Outline every malaria parasite.
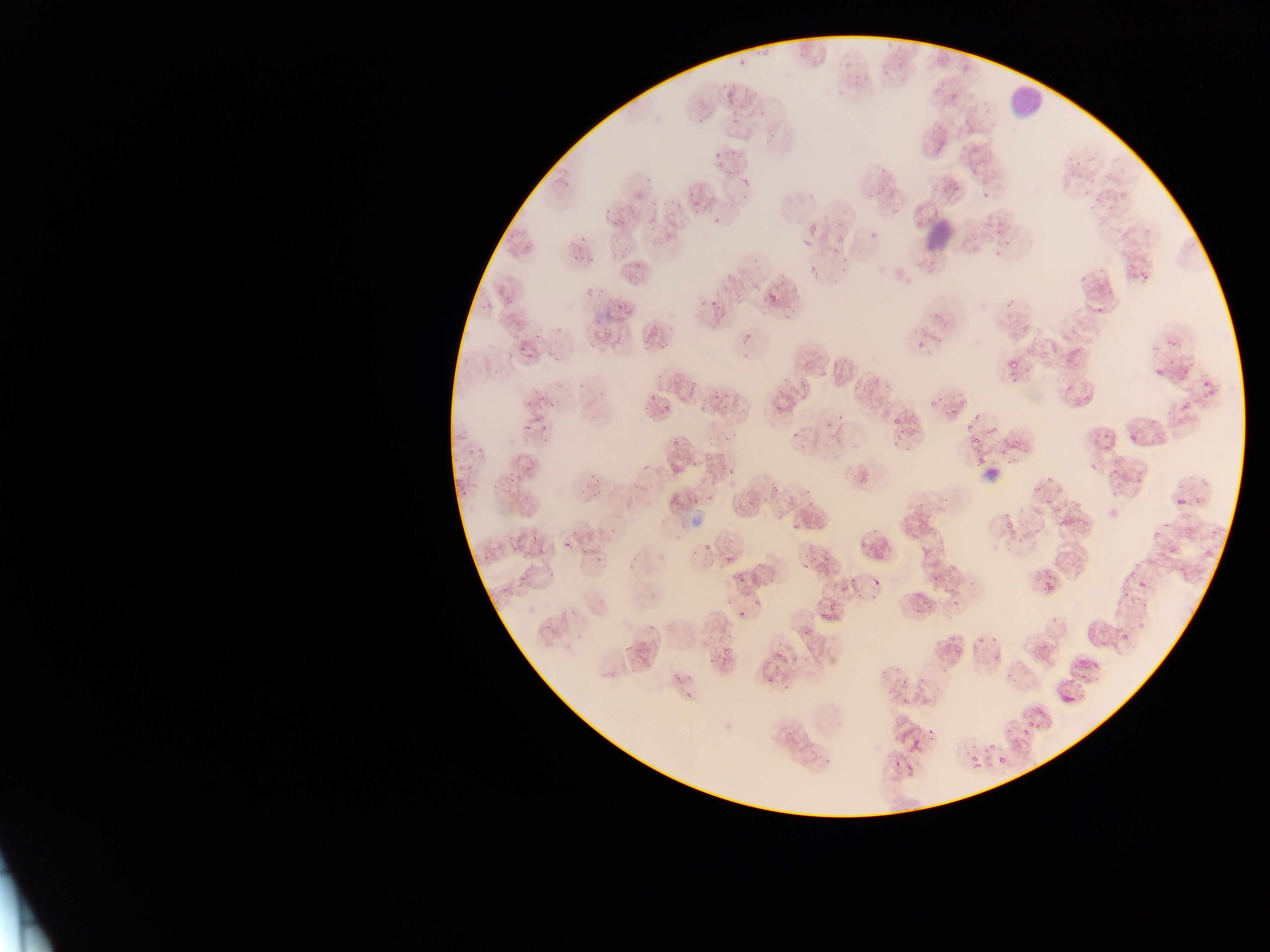
Approximate bounding boxes as (left, top, right, bottom) in pixels.
Malaria parasites: (948, 84, 976, 108), (1066, 153, 1088, 171), (637, 180, 671, 208), (687, 193, 706, 211), (978, 193, 986, 203), (794, 210, 827, 248), (604, 212, 622, 234), (714, 213, 728, 230), (661, 222, 685, 236), (986, 223, 1018, 244), (513, 231, 534, 266), (610, 244, 632, 260), (569, 249, 582, 263), (620, 276, 644, 287), (493, 281, 522, 318), (761, 286, 786, 303), (710, 295, 717, 306), (594, 314, 618, 335), (739, 322, 761, 336), (644, 324, 657, 338), (551, 338, 568, 352), (1172, 338, 1202, 378), (1145, 341, 1176, 379), (516, 343, 532, 357), (1005, 351, 1026, 377), (493, 352, 517, 379), (777, 372, 816, 401), (852, 379, 862, 391), (1179, 384, 1197, 416), (1200, 384, 1222, 402), (531, 389, 556, 416), (707, 394, 729, 412), (654, 396, 671, 410), (927, 396, 937, 408), (968, 396, 988, 430), (771, 400, 785, 413), (828, 408, 845, 427), (888, 408, 906, 438), (518, 418, 533, 437), (1125, 426, 1139, 450), (966, 429, 980, 446), (669, 434, 679, 446), (704, 445, 714, 459), (497, 450, 539, 496), (968, 451, 986, 476), (1103, 451, 1134, 473), (459, 459, 471, 483), (729, 459, 739, 476), (1026, 472, 1061, 498), (772, 478, 782, 491), (588, 479, 603, 497), (912, 485, 942, 509), (1172, 495, 1191, 510), (786, 512, 806, 536), (998, 512, 1021, 535), (924, 514, 937, 536), (508, 531, 529, 549), (700, 538, 718, 554), (562, 540, 573, 552), (590, 547, 616, 563), (804, 550, 820, 561), (926, 561, 954, 598), (1042, 563, 1072, 589), (1132, 566, 1156, 588), (871, 571, 889, 586), (734, 573, 744, 583), (841, 582, 857, 594), (1119, 582, 1132, 598), (499, 584, 512, 599), (823, 585, 851, 616), (906, 597, 930, 624), (737, 601, 760, 620), (800, 621, 818, 639), (981, 626, 998, 644), (626, 630, 650, 649), (947, 632, 960, 651), (717, 644, 727, 657), (985, 645, 1001, 663), (772, 647, 784, 661), (938, 648, 957, 677), (1069, 656, 1087, 674), (767, 662, 786, 684), (889, 687, 912, 702), (1053, 688, 1084, 699), (1020, 715, 1038, 732), (780, 726, 795, 740), (964, 726, 996, 776), (800, 735, 820, 756), (899, 735, 921, 756), (994, 748, 1012, 766).

Leukocyte locations: (1012, 73, 1053, 119), (923, 205, 965, 265). Image is 1270×952 pixels. One field of view. Thin blood smear. Photographed through a microscope with a mobile-phone camera. Sample from Ghana.